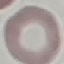
result: negative for malaria parasites
stain: Giemsa
capture: smartphone camera at the microscope eyepiece
preparation: thin smear
image_type: automatically extracted cell patch, resized to 64 × 64 pixels